Assess this cell for malaria.
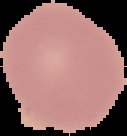
It is uninfected.

image size = 127×136 pixels
image type = cell region segmented out of the field of view; surrounding area masked to black
preparation = thin blood film